Classify this cell by malaria status.
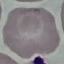
It is uninfected.

Summary:
  - Preparation: thin smear
  - Capture: smartphone through the microscope eyepiece
  - Image type: cell patch, automatically extracted from a larger field of view and resized to 64 × 64 pixels
  - Stain: Giemsa